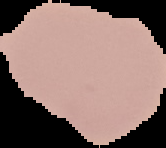

Summary:
  - Preparation: thin blood smear
  - Image type: segmented cell region on a black background
  - Result: negative for malaria parasites
  - Image size: 166×148 pixels